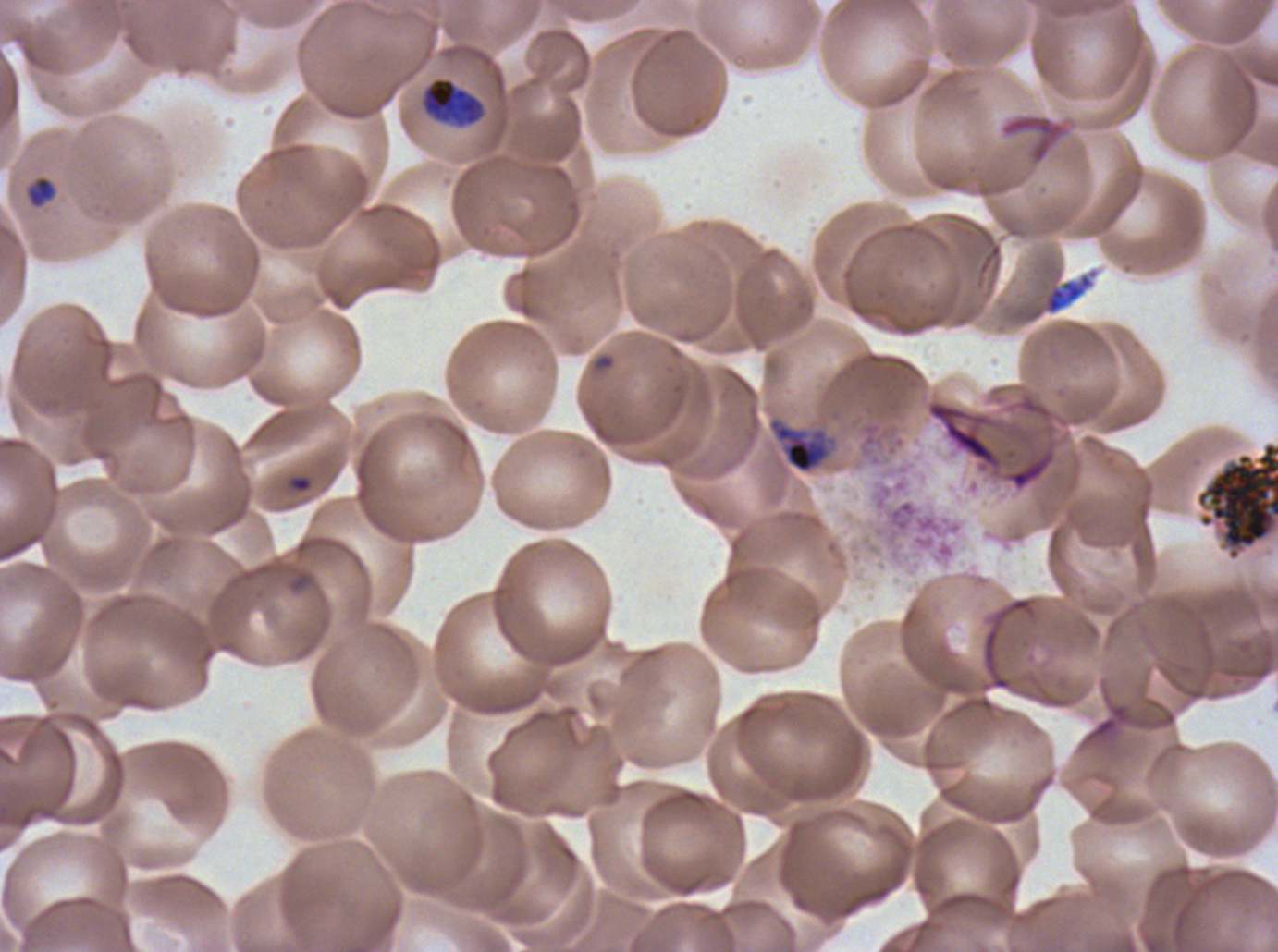
debris_locations: 'approximate bounding boxes as [x1, y1, x2, y2] in pixels: [1000, 114, 1070, 165], [1043, 273, 1094, 315], [1195, 441, 1277, 561]'
preparation: thin blood film
ring_locations: 'approximate bounding boxes as [x1, y1, x2, y2] in pixels: [287, 474, 313, 494]'
late_trophozoite_locations: 'approximate bounding boxes as [x1, y1, x2, y2] in pixels: [767, 416, 832, 474]'
image_size: 1278×952 pixels
specimen: P. falciparum cultured ex vivo for 24 to 48 hours, from a patient in The Gambia
field_of_view: sub-image separated from a larger composite
early_schizont_locations: 'approximate bounding boxes as [x1, y1, x2, y2] in pixels: [423, 77, 481, 124]'
life_cycle_stages_observed: ring, late-ring/early-trophozoite, late trophozoite, early schizont
late_ring_early_trophozoite_locations: 'approximate bounding boxes as [x1, y1, x2, y2] in pixels: [28, 176, 55, 208]'
stain: Giemsa